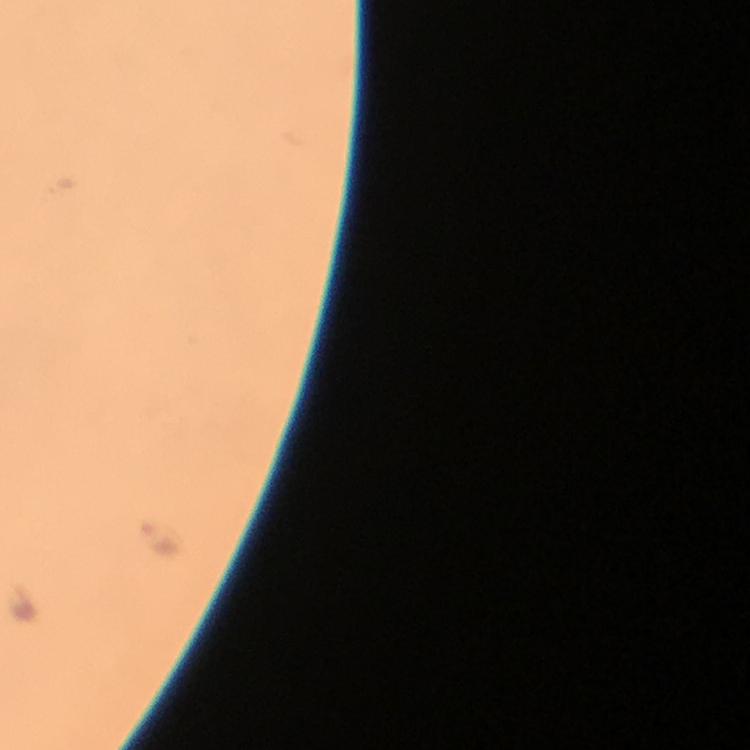
cropped from = one field of view
Plasmodium parasite locations = approximate centers as (x, y) in pixels: (154, 538)
preparation = thick blood smear
image size = 750×750 pixels
context = from a diagnostic examination for malaria
capture = smartphone camera through the microscope
immersion oil = used
stain = Giemsa
magnification = 100x